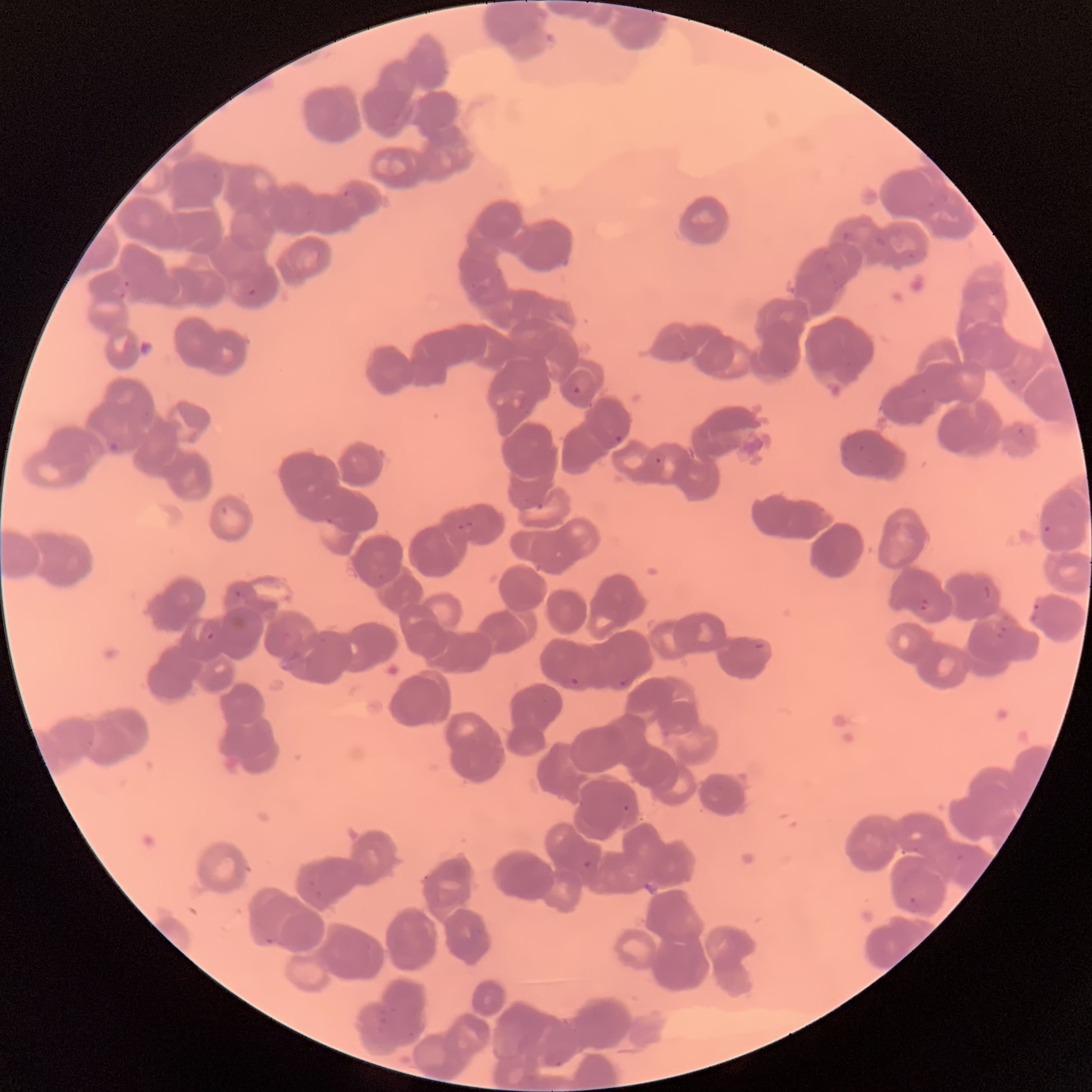
Approximate bounding boxes as (x1,y1)-(x2,y2) corner pairs in pixels. Plasmodium parasites too small for a box (approximate centers as (x,y) in pixels): (540,506), (626,808). Plasmodium parasite locations: (342,189)-(350,198), (122,279)-(130,287), (247,288)-(256,296), (571,385)-(582,395), (613,435)-(623,443), (107,440)-(121,454), (654,457)-(662,464), (325,516)-(334,525), (457,521)-(477,533), (1044,525)-(1051,533), (983,585)-(992,599), (234,589)-(243,598), (920,597)-(929,612), (1030,602)-(1040,622), (997,625)-(1007,639), (206,631)-(215,640), (569,675)-(580,686), (618,679)-(627,687), (583,860)-(594,869), (909,896)-(917,904). Thin blood smear. Image is 1092×1092 pixels. The red blood cells show rouleaux formation. Light microscopy.